Identify the parasite.
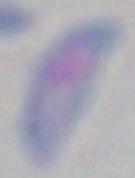

This is Toxoplasma gondii.

modality = micrograph
magnification = 1000x